Assess the morphology of the erythrocytes.
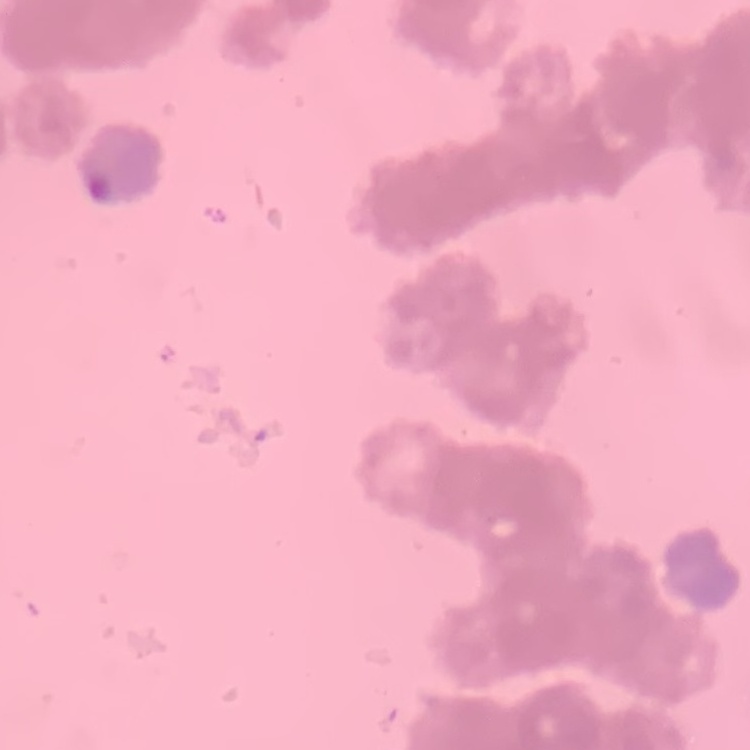
Rouleaux formation.

stain: Field's or Giemsa
preparation: thin peripheral smear
image_type: one tile cut from a larger photomicrograph